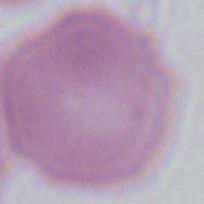 Photomicrograph. 1000x magnification. An erythrocyte is seen.